Assess the morphology of the red blood cells.
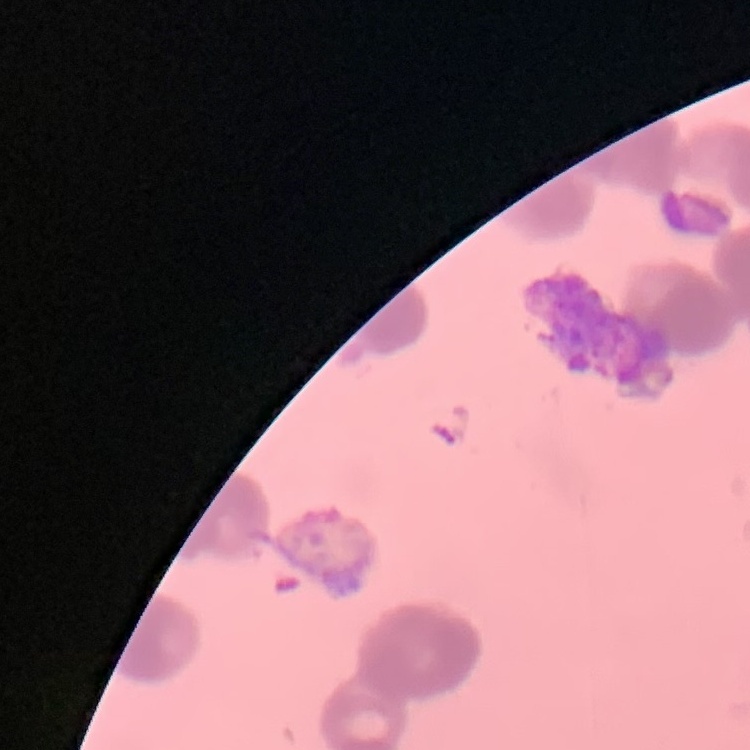

Rouleaux formation.

{
  "preparation": "thin blood film",
  "image_type": "one tile cut from a larger photomicrograph",
  "stain": "Field's or Giemsa"
}